State which parasite is depicted.
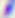

This is Toxoplasma gondii.

Photomicrograph. 400x magnification.